Describe the morphology of the erythrocytes.
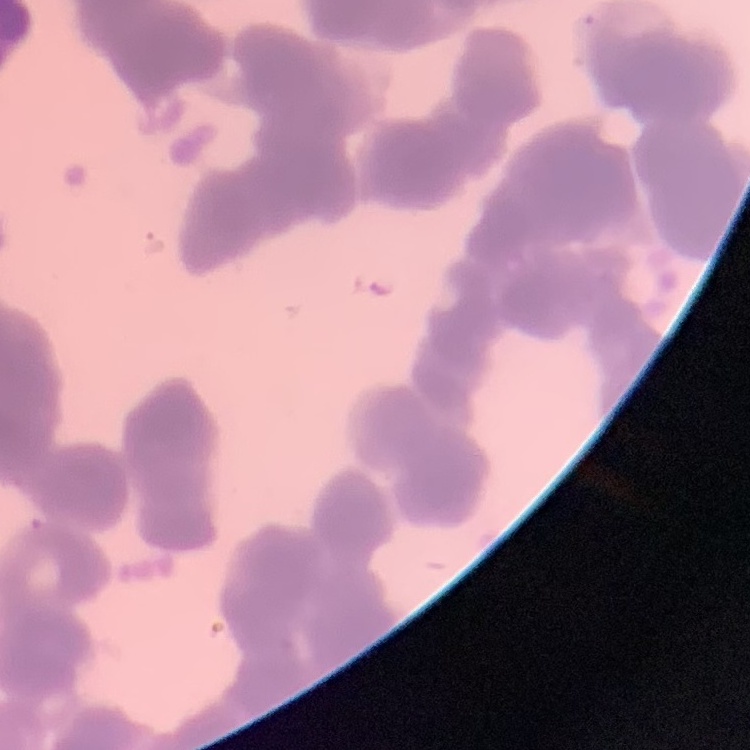
Rouleaux formation.

Stained with either Field's or Giemsa. Thin blood smear. Square crop of a larger photomicrograph.